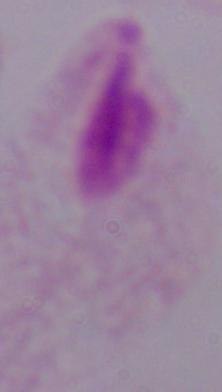
Micrograph. 1000x magnification. A trichomonad is seen.